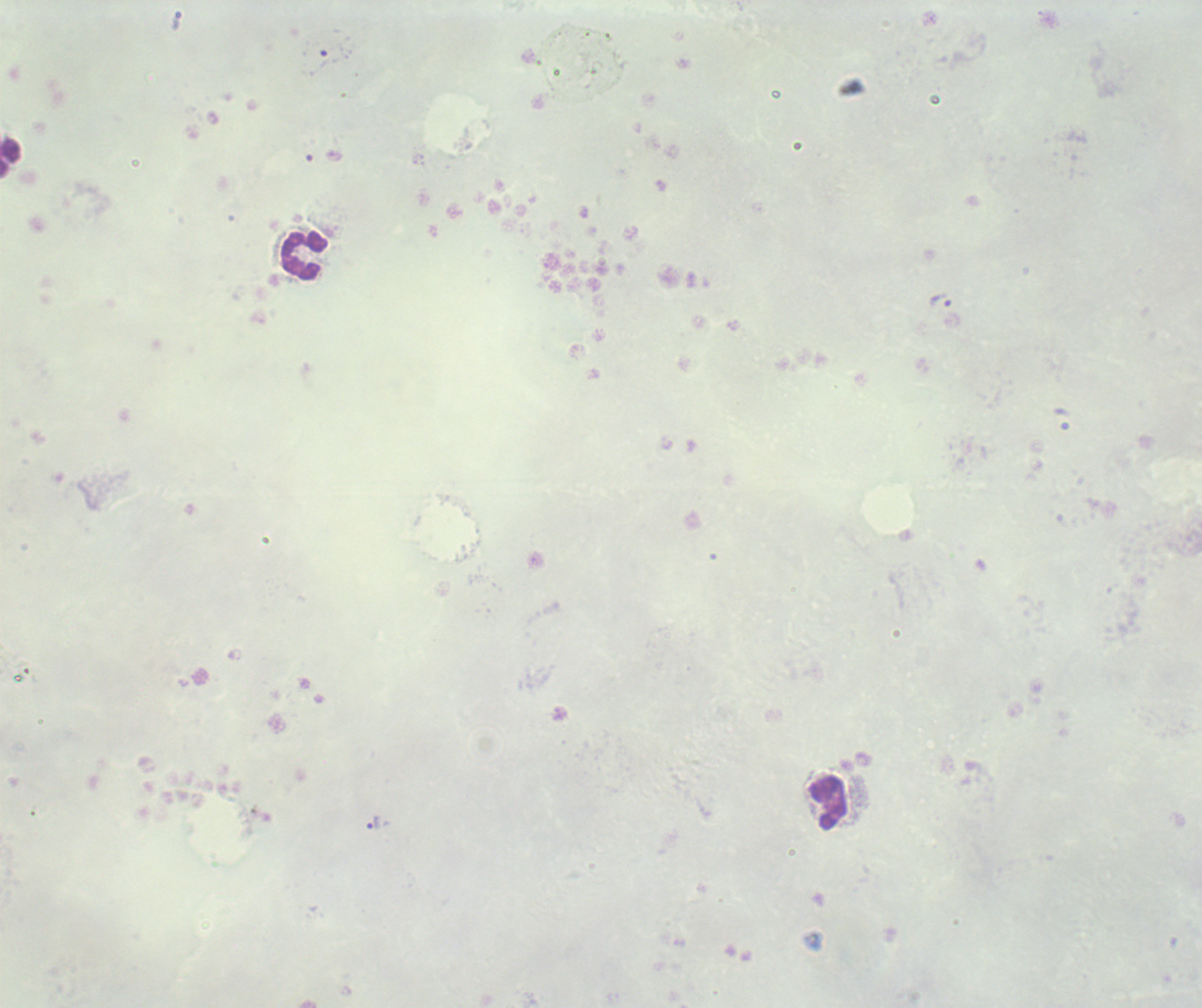

Approximate centers as (x, y) in pixels.
Summary:
  - Leukocyte locations: (11, 159), (303, 256), (827, 803)
  - Trophozoite locations: (939, 301), (374, 823)
  - Result: malaria parasites identified
  - Image size: 1202×1008 pixels
  - Stain: Romanowsky
  - Background quality: unsatisfactory
  - Coloration quality: bad
  - Field of view: single
  - Context: previously used in an actual diagnosis
  - Magnification: 100x
  - Preparation: thick smear of blood